Describe the morphology of the erythrocytes.
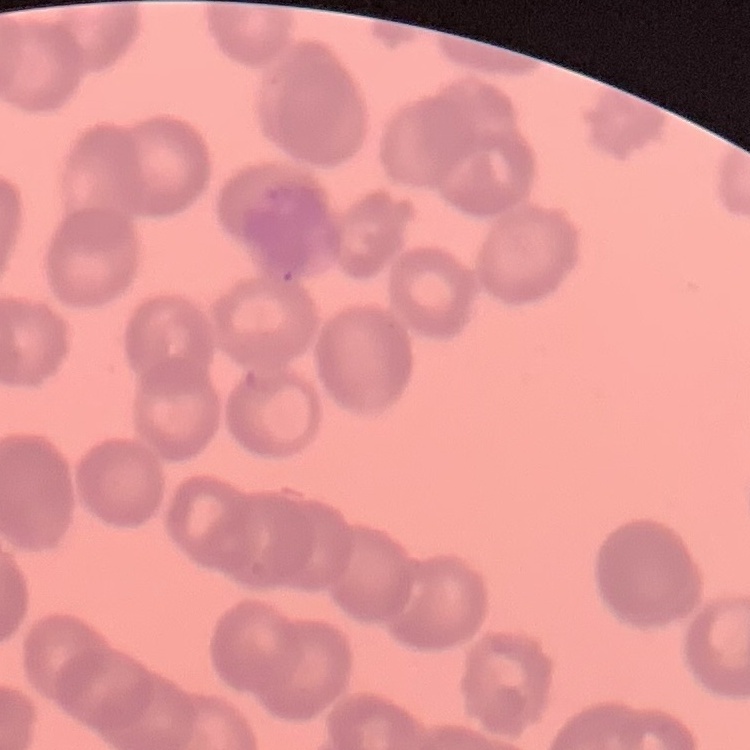
They show rouleaux formation.

Stained with either Field's or Giemsa. Square crop of a larger photomicrograph. Thin peripheral smear.